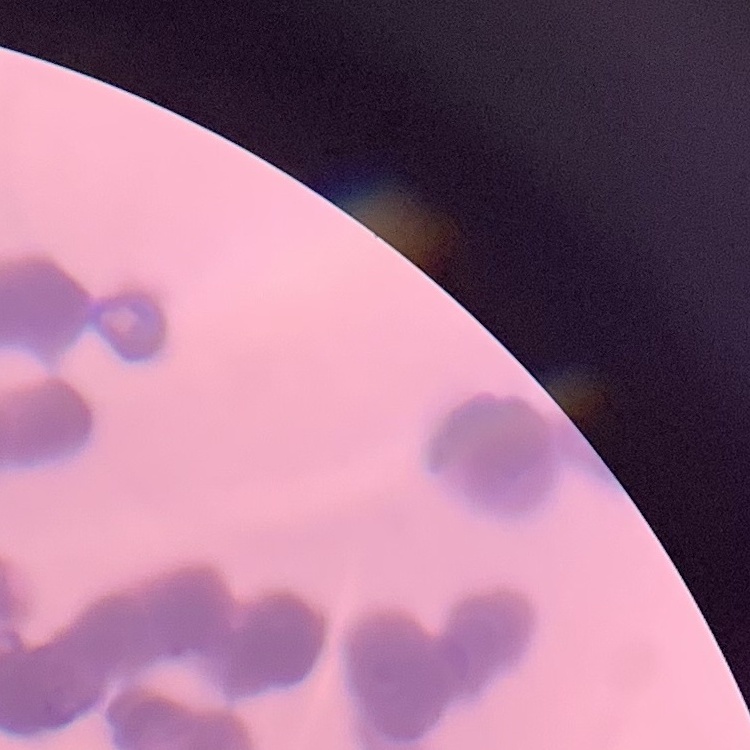
Summary:
  - Erythrocyte morphology: rouleaux formation
  - Preparation: thin peripheral smear
  - Image type: square crop of a larger photomicrograph
  - Stain: Field's or Giemsa